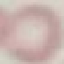
Result: no malaria parasites seen. Giemsa stain. Photographed with a smartphone camera at the microscope eyepiece. Thin smear of blood. Cell patch, automatically extracted from a larger field of view and resized to 64 × 64 pixels.